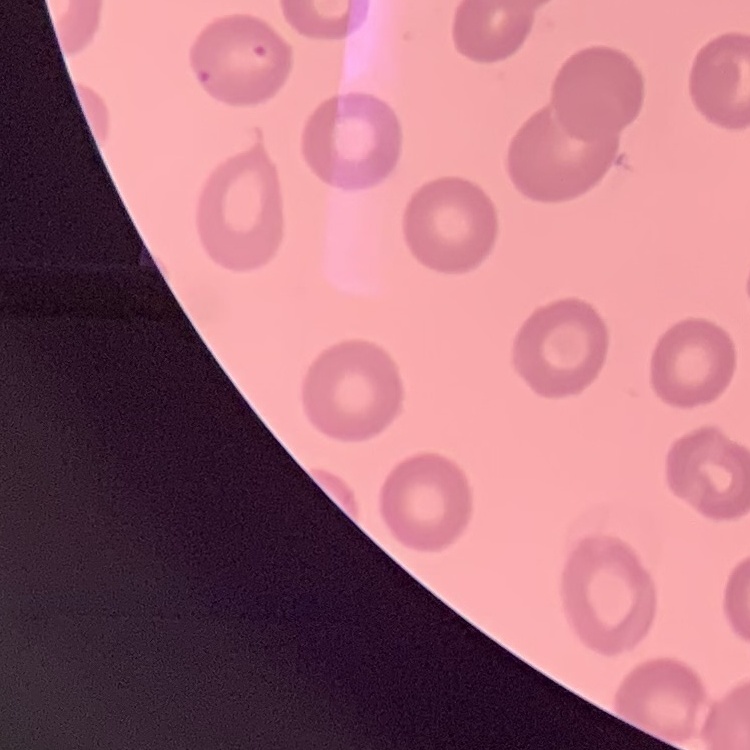
The erythrocytes exhibit no rouleaux formation. Field's or Giemsa stain. Square crop of a larger photomicrograph. Thin blood film.